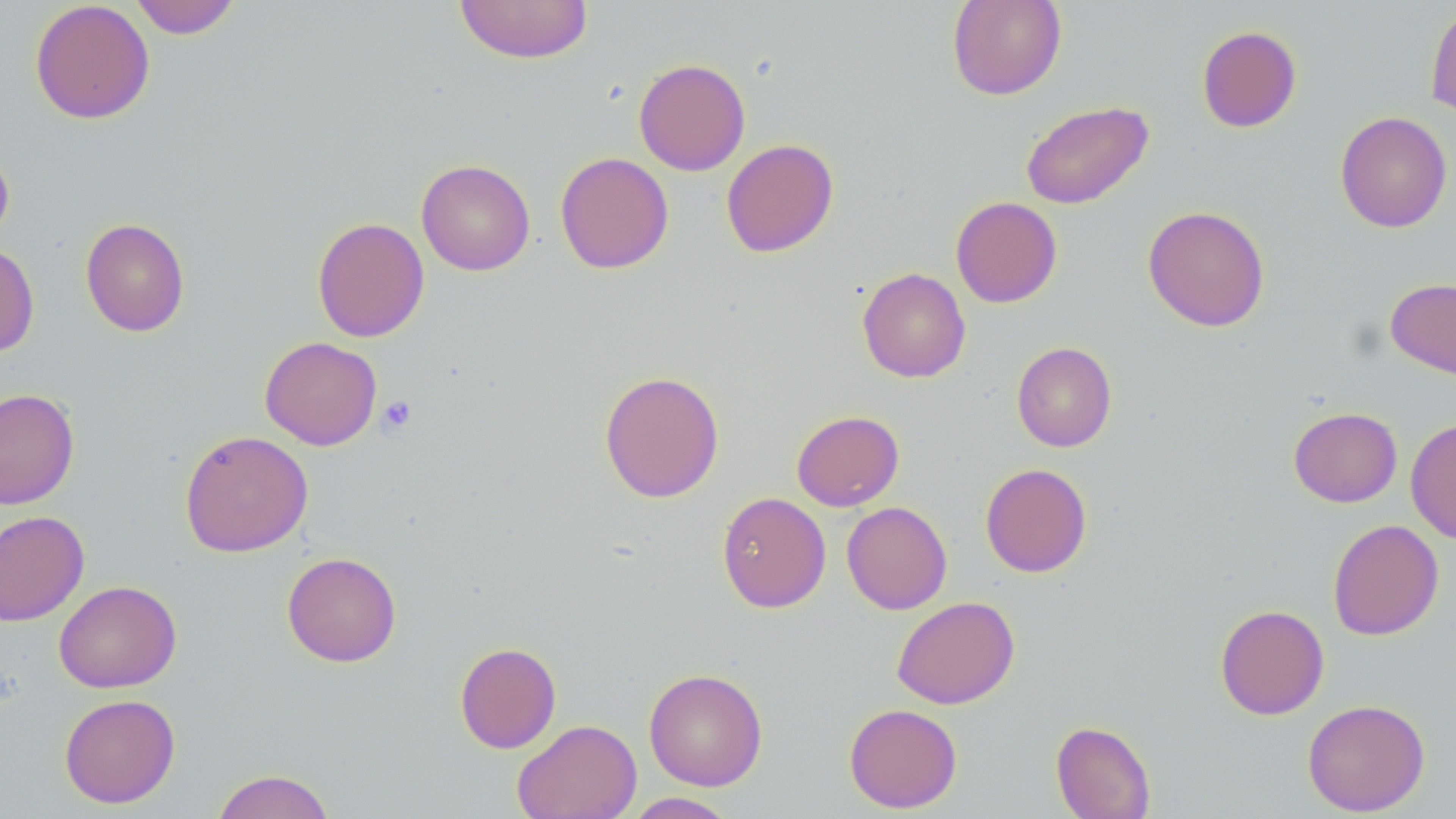

slide-level diagnosis = no evidence of blood parasites
platelet locations = approximate bounding boxes as named x1/y1/x2/y2 corners in pixels: (x1=376, y1=395, x2=418, y2=436)
preparation = thin blood film
stain = May-Grünwald-Giemsa
image size = 1456×819 pixels
magnification = 1000x
modality = light microscopy
uninfected red blood cell locations = approximate bounding boxes as named x1/y1/x2/y2 corners in pixels: (x1=128, y1=0, x2=242, y2=39), (x1=454, y1=0, x2=594, y2=64), (x1=946, y1=0, x2=1067, y2=100), (x1=29, y1=1, x2=155, y2=125), (x1=1425, y1=3, x2=1456, y2=119), (x1=1196, y1=25, x2=1302, y2=132), (x1=634, y1=58, x2=751, y2=176), (x1=1020, y1=100, x2=1154, y2=209), (x1=1334, y1=111, x2=1453, y2=233), (x1=721, y1=138, x2=838, y2=258), (x1=0, y1=142, x2=15, y2=246), (x1=554, y1=152, x2=674, y2=274), (x1=416, y1=158, x2=536, y2=276), (x1=950, y1=196, x2=1062, y2=308), (x1=1143, y1=205, x2=1270, y2=332), (x1=80, y1=217, x2=190, y2=337), (x1=312, y1=217, x2=429, y2=343), (x1=0, y1=242, x2=39, y2=357), (x1=857, y1=267, x2=971, y2=382), (x1=1385, y1=277, x2=1456, y2=380), (x1=260, y1=336, x2=382, y2=450), (x1=1012, y1=341, x2=1117, y2=452), (x1=599, y1=370, x2=725, y2=503), (x1=0, y1=388, x2=79, y2=509), (x1=1288, y1=407, x2=1402, y2=507), (x1=791, y1=409, x2=904, y2=511), (x1=1405, y1=417, x2=1456, y2=544), (x1=179, y1=430, x2=313, y2=557), (x1=980, y1=463, x2=1092, y2=578), (x1=716, y1=492, x2=831, y2=613), (x1=841, y1=501, x2=952, y2=614), (x1=0, y1=510, x2=89, y2=626), (x1=1327, y1=519, x2=1444, y2=641), (x1=281, y1=551, x2=402, y2=667), (x1=53, y1=579, x2=181, y2=693), (x1=892, y1=596, x2=1019, y2=710), (x1=1214, y1=604, x2=1329, y2=720), (x1=454, y1=642, x2=562, y2=753), (x1=643, y1=667, x2=768, y2=791), (x1=59, y1=693, x2=181, y2=808), (x1=1302, y1=698, x2=1430, y2=816), (x1=844, y1=703, x2=962, y2=813), (x1=512, y1=719, x2=641, y2=819), (x1=1051, y1=720, x2=1156, y2=818), (x1=211, y1=769, x2=336, y2=819), (x1=622, y1=792, x2=738, y2=818)
field of view = one of a larger specimen